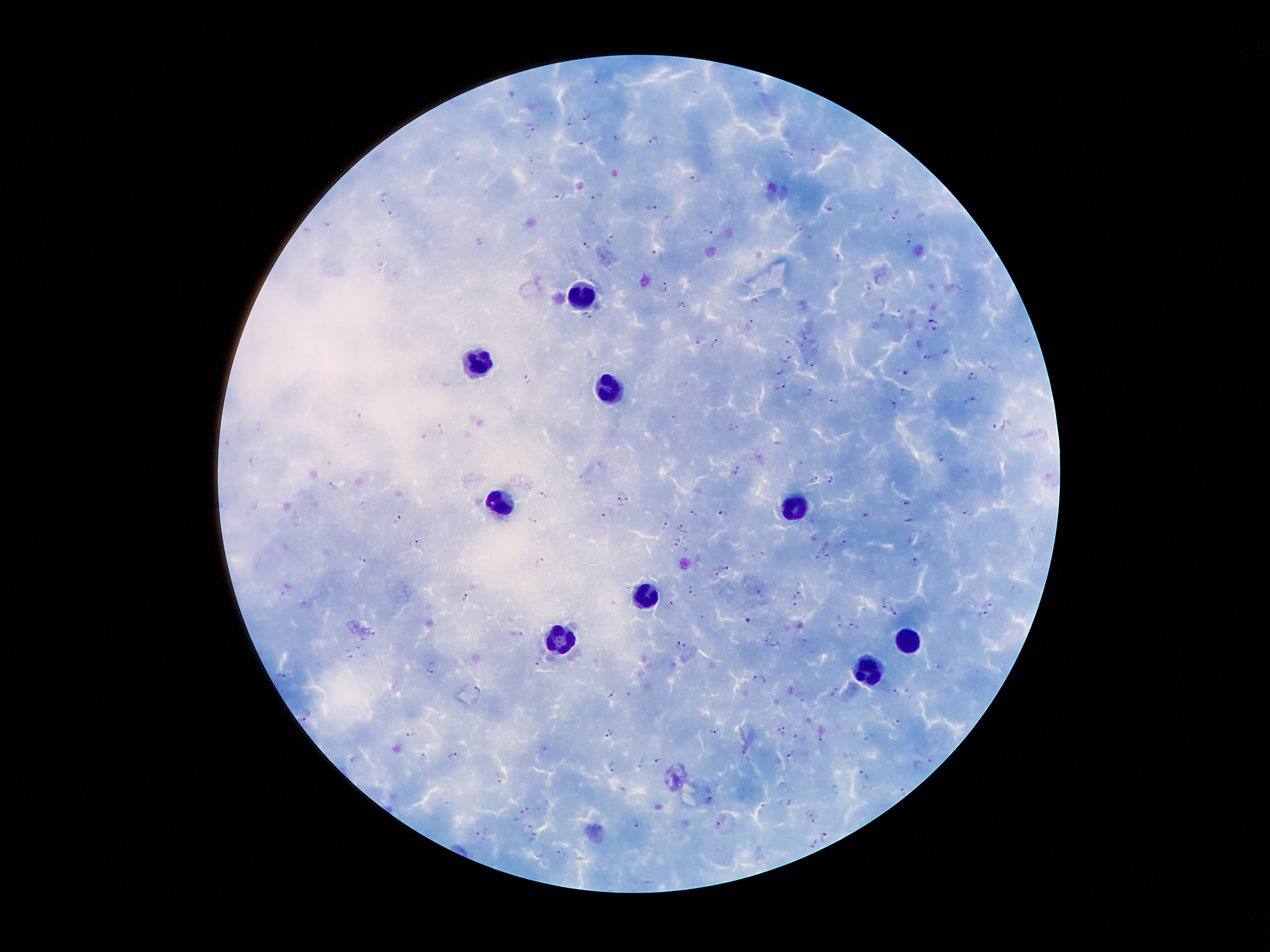 Approximate object centers, in pixels from the top-left corner. Plasmodium parasite locations: (x=598, y=77), (x=586, y=114), (x=571, y=121), (x=532, y=125), (x=655, y=141), (x=586, y=143), (x=814, y=151), (x=786, y=153), (x=693, y=178), (x=559, y=195), (x=598, y=196), (x=384, y=198), (x=650, y=208), (x=827, y=208), (x=395, y=215), (x=896, y=215), (x=800, y=227), (x=708, y=230), (x=909, y=235), (x=610, y=239), (x=479, y=242), (x=380, y=245), (x=588, y=246), (x=657, y=255), (x=840, y=257), (x=381, y=267), (x=869, y=285), (x=664, y=286), (x=755, y=302), (x=683, y=304), (x=900, y=313), (x=588, y=316), (x=934, y=323), (x=751, y=324), (x=804, y=339), (x=698, y=340), (x=716, y=342), (x=789, y=342), (x=928, y=356), (x=788, y=358), (x=811, y=361), (x=782, y=370), (x=907, y=370), (x=973, y=375), (x=526, y=378), (x=783, y=387), (x=903, y=391), (x=810, y=392), (x=970, y=399), (x=835, y=400), (x=892, y=404), (x=732, y=426), (x=1001, y=426), (x=442, y=428), (x=228, y=439), (x=939, y=456), (x=254, y=462), (x=739, y=466), (x=734, y=472), (x=814, y=477), (x=830, y=478), (x=334, y=487), (x=622, y=495), (x=542, y=496), (x=907, y=502), (x=365, y=504), (x=967, y=511), (x=608, y=512), (x=865, y=513), (x=692, y=514), (x=720, y=514), (x=398, y=520), (x=532, y=520), (x=665, y=523), (x=682, y=528), (x=842, y=539), (x=677, y=542), (x=418, y=543), (x=828, y=552), (x=820, y=556), (x=364, y=559), (x=541, y=560), (x=916, y=561), (x=725, y=567), (x=714, y=572), (x=692, y=591), (x=760, y=593), (x=798, y=594), (x=466, y=596), (x=885, y=600), (x=304, y=604), (x=672, y=604), (x=990, y=604), (x=794, y=605), (x=896, y=612), (x=982, y=615), (x=837, y=619), (x=854, y=627), (x=373, y=632), (x=518, y=634), (x=765, y=638), (x=682, y=646), (x=775, y=646), (x=351, y=653), (x=540, y=664), (x=430, y=669), (x=283, y=677), (x=759, y=679), (x=477, y=689), (x=611, y=692), (x=836, y=692), (x=894, y=694), (x=910, y=694), (x=304, y=717), (x=899, y=724), (x=782, y=727), (x=715, y=730), (x=610, y=732), (x=413, y=734), (x=823, y=736), (x=798, y=738), (x=871, y=738), (x=546, y=749), (x=746, y=749), (x=452, y=753), (x=793, y=755), (x=425, y=756), (x=355, y=758), (x=659, y=759), (x=933, y=760), (x=642, y=765), (x=919, y=765), (x=614, y=766), (x=864, y=775), (x=500, y=776), (x=836, y=788), (x=623, y=791), (x=901, y=794), (x=709, y=800), (x=786, y=803), (x=546, y=804), (x=528, y=806), (x=538, y=810), (x=522, y=812), (x=814, y=816), (x=635, y=823), (x=718, y=825), (x=526, y=827), (x=475, y=833), (x=534, y=837), (x=825, y=837), (x=562, y=851). Leukocyte locations: (x=586, y=293), (x=486, y=365), (x=609, y=385), (x=504, y=506), (x=794, y=506), (x=646, y=594), (x=565, y=637), (x=912, y=639), (x=870, y=671). 100x magnification. Thick peripheral-blood smear. Image is 1270×952 pixels. Giemsa stain. Single field of view. Photographed through the microscope eyepiece with a smartphone camera. Patient malaria status: positive for Plasmodium falciparum.